Evaluate for malaria.
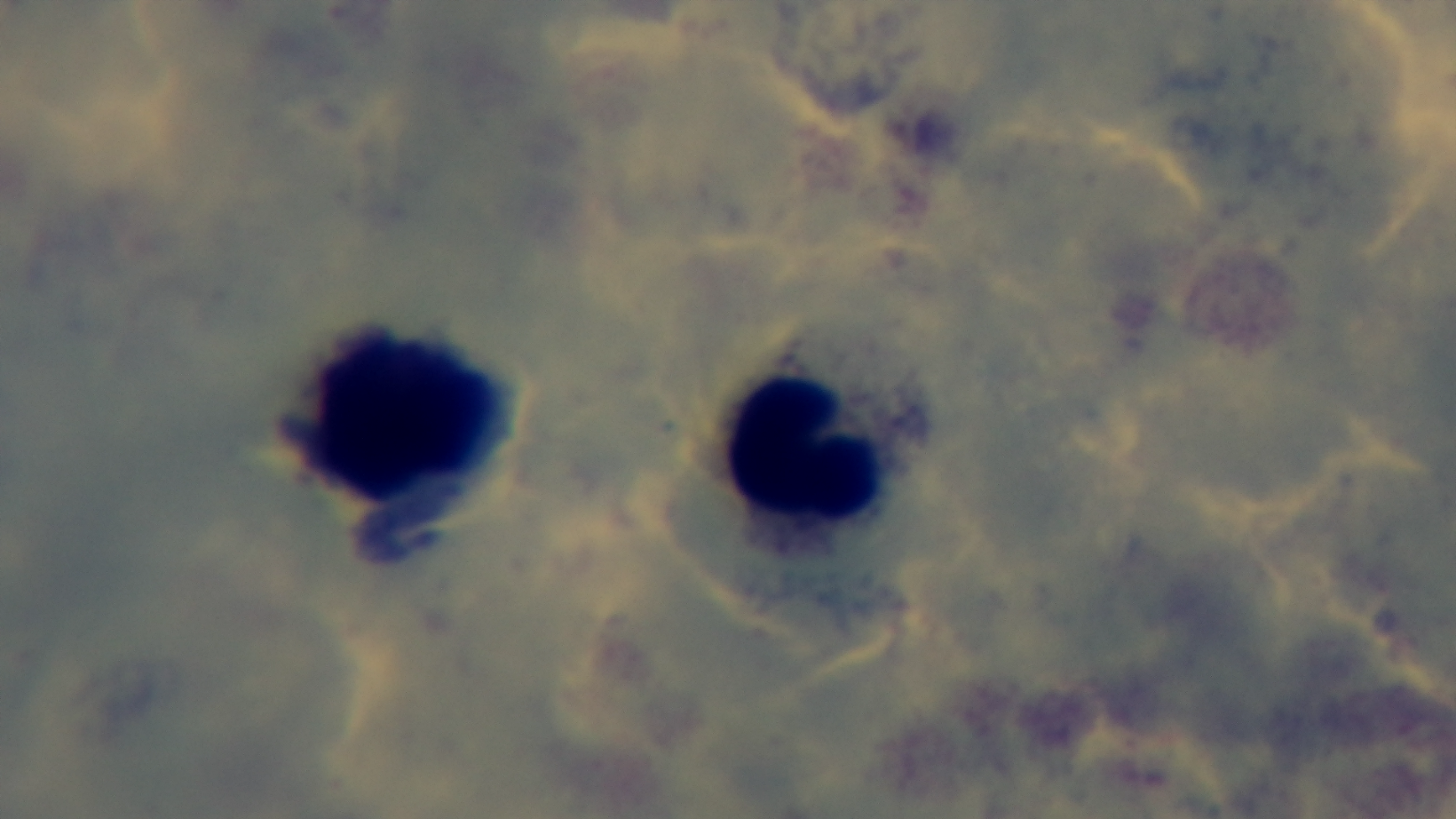

Negative.

Summary:
  - Objective: 100x oil immersion
  - Field of view: one from the slide
  - Modality: light microscopy
  - Stain: Giemsa
  - Capture: mounted 4K digital camera
  - Preparation: thick blood film